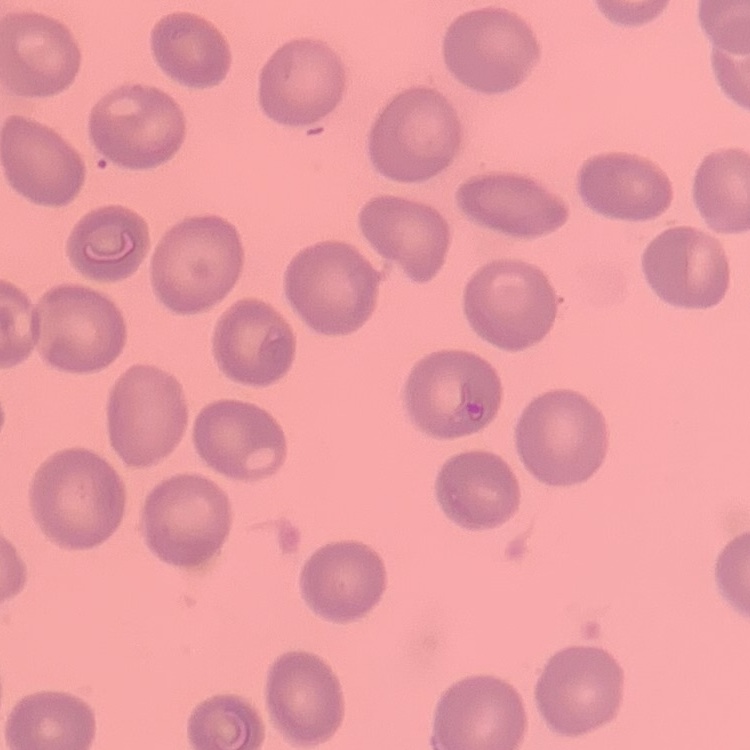
The erythrocytes exhibit no rouleaux formation. Field's or Giemsa stain. Thin blood smear. Square crop of a larger photomicrograph.